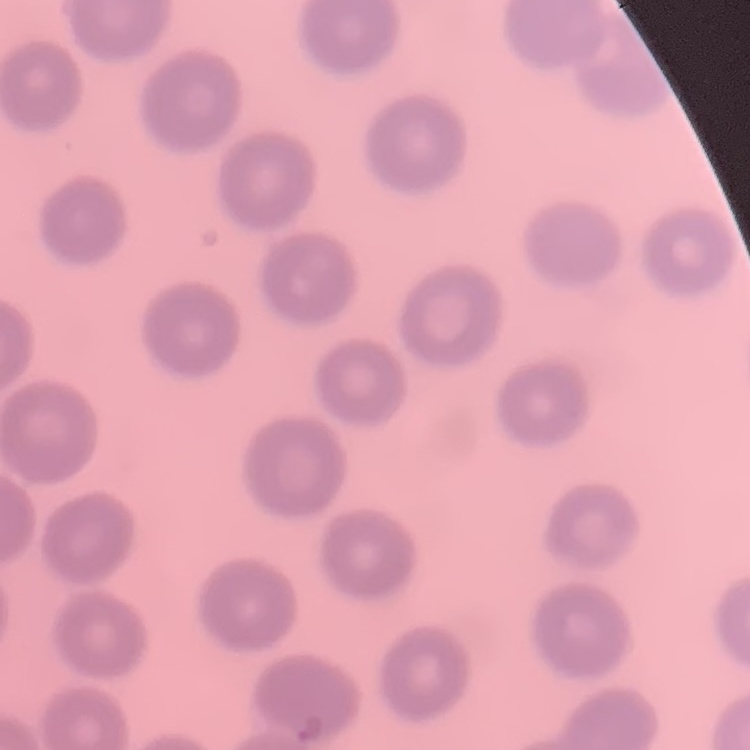
The erythrocytes exhibit no rouleaux formation. Stained with either Field's or Giemsa. Thin peripheral smear. One tile cut from a larger photomicrograph.